Point out each Plasmodium parasite.
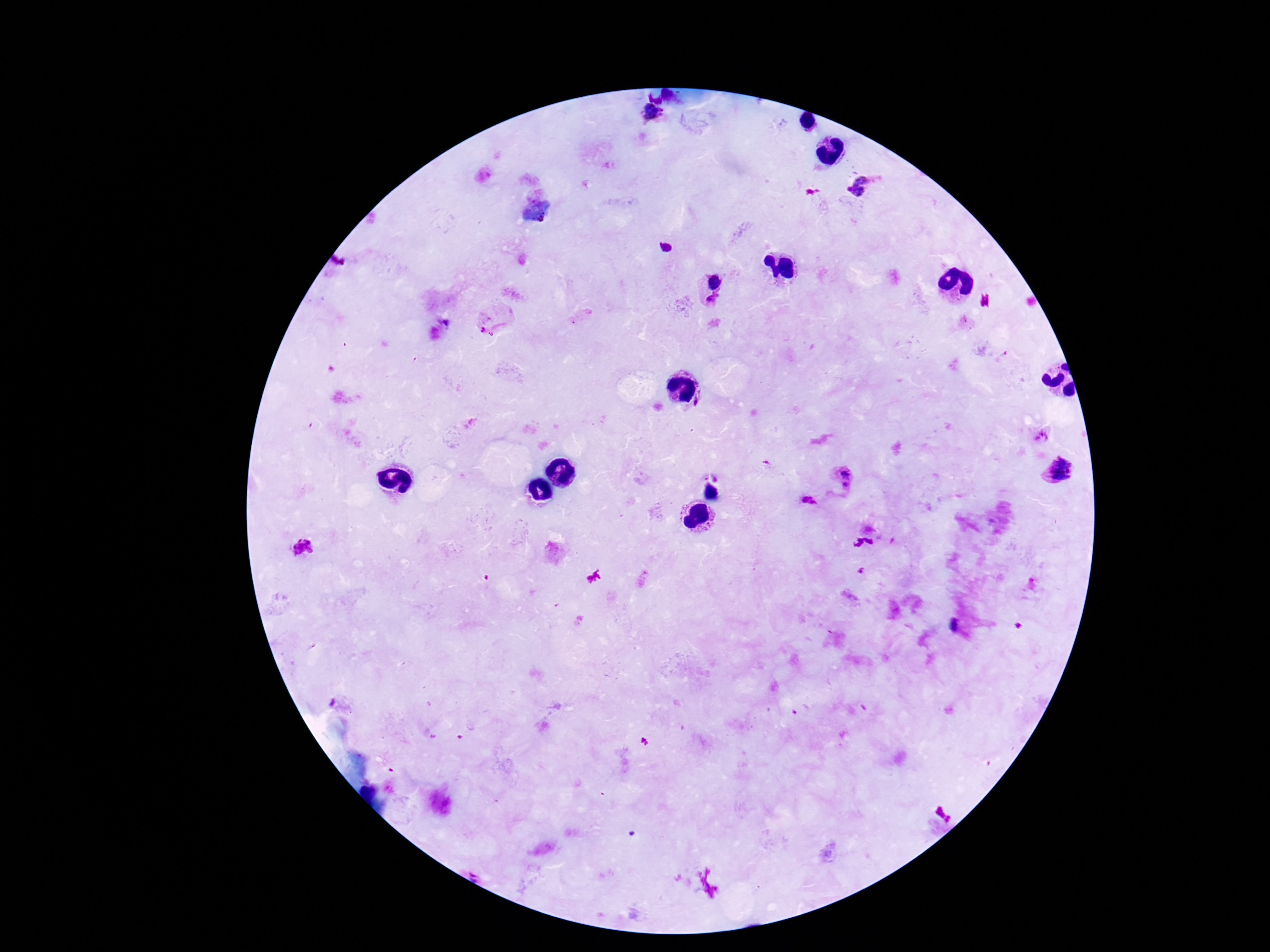
Approximate object centers, in pixels from the top-left corner.
Plasmodium parasites: (x=661, y=110), (x=649, y=112), (x=661, y=115), (x=861, y=186), (x=665, y=248), (x=716, y=281), (x=712, y=299), (x=489, y=320), (x=699, y=402), (x=1060, y=470), (x=845, y=472), (x=847, y=484), (x=809, y=502), (x=303, y=547), (x=955, y=625).

Photographed through the microscope eyepiece with a smartphone camera. Giemsa-stained preparation. Image is 1270×952 pixels. Patient malaria status: positive. Thick blood film. One field from this slide. 100x magnification.